State which parasite is depicted.
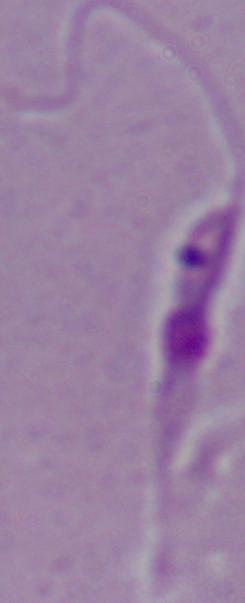
This is Leishmania.

Micrograph. Captured at 1000x magnification.